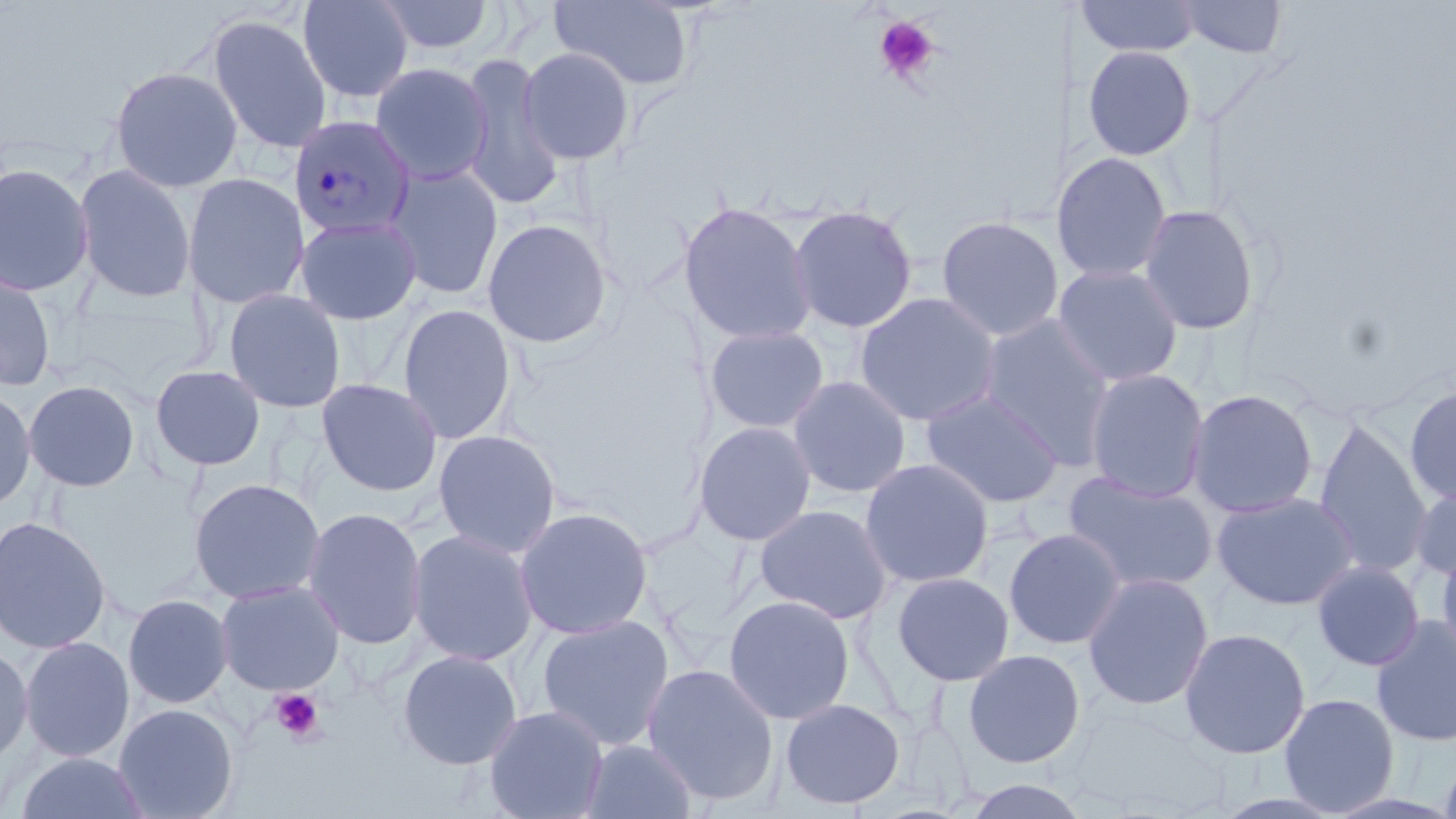

slide_level_diagnosis: Plasmodium malariae
modality: optical microscopy
preparation: thin blood film
image_size: 1456×819 pixels
platelet_locations: 'approximate bounding boxes as (x1,y1)-(x2,y2) corner pairs in pixels: (873,15)-(940,84), (269,688)-(325,743)'
uninfected_red_blood_cell_locations: 'approximate bounding boxes as (x1,y1)-(x2,y2) corner pairs in pixels: (297,0)-(414,103), (372,0)-(497,57), (550,0)-(695,92), (1076,0)-(1203,58), (1174,0)-(1288,59), (206,14)-(332,154), (1082,45)-(1197,161), (518,46)-(636,165), (457,53)-(564,211), (369,60)-(492,188), (109,65)-(243,194), (1058,151)-(1173,284), (0,161)-(95,297), (73,162)-(197,304), (383,165)-(504,300), (182,172)-(309,309), (678,201)-(817,347), (1137,203)-(1262,336), (787,204)-(918,334), (294,215)-(423,325), (935,215)-(1061,342), (481,218)-(614,349), (1052,263)-(1184,388), (0,268)-(57,391), (223,289)-(346,413), (854,292)-(1001,427), (397,303)-(517,445), (979,315)-(1118,467), (704,324)-(830,435), (149,364)-(266,471), (1084,368)-(1210,503), (788,375)-(912,499), (316,378)-(443,498), (23,380)-(141,492), (1405,383)-(1456,507), (0,387)-(36,512), (1185,388)-(1319,519), (921,390)-(1064,508), (1314,419)-(1433,578), (693,421)-(817,546), (432,429)-(562,559), (859,457)-(995,588), (1063,470)-(1217,595), (188,477)-(326,605), (1410,483)-(1456,584), (1212,491)-(1359,610), (754,504)-(894,624), (302,506)-(428,649), (514,506)-(654,640), (0,516)-(111,654), (1003,528)-(1127,650), (407,529)-(539,666), (1436,542)-(1456,667), (1311,560)-(1425,671), (891,571)-(1015,686), (1082,572)-(1214,710), (215,580)-(345,696), (123,593)-(234,709), (723,594)-(855,724), (535,613)-(675,751), (1371,617)-(1456,747), (1179,628)-(1310,759), (19,636)-(135,762), (0,643)-(33,766), (963,648)-(1086,768), (397,649)-(522,770), (642,663)-(780,805), (1279,693)-(1400,815), (780,698)-(905,809), (114,703)-(239,819), (483,705)-(608,819), (581,738)-(699,818), (1438,744)-(1456,819), (15,752)-(150,819), (961,778)-(1090,818)'
plasmodium_malariae_infected_red_blood_cell_locations: 'approximate bounding boxes as (x1,y1)-(x2,y2) corner pairs in pixels: (288,115)-(415,239)'
stain: May-Grünwald-Giemsa
magnification: 1000x
field_of_view: single